Classify this cell by malaria status.
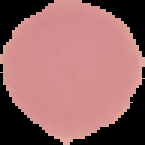
Uninfected.

image type = segmented cell region with the area outside set to black
preparation = thin blood smear
image size = 145×145 pixels